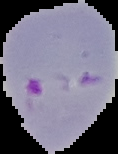

Result: malaria parasites detected. Image is 118×154 pixels. Segmented cell region on a black background. From a thin blood film.